State the preparation type.
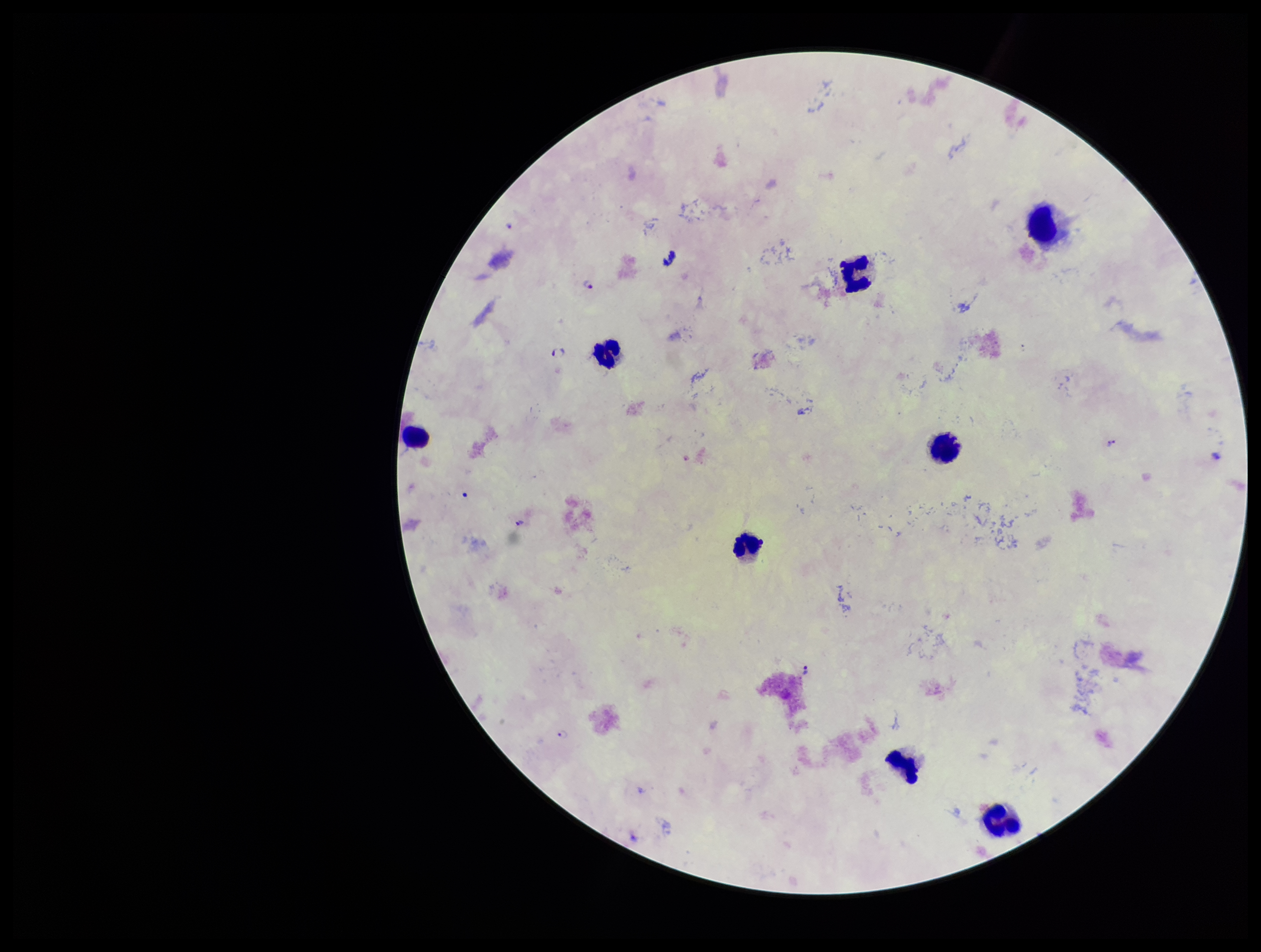

Thick.

Summary:
  - Image size: 1261×952 pixels
  - Patient malaria status: infected
  - Leukocyte count: 8
  - Species reported for this patient: Plasmodium falciparum
  - Field of view: one from this slide
  - Plasmodium parasites: identified
  - Capture: smartphone photograph through the microscope eyepiece
  - Parasite count: 7
  - Stain: Giemsa